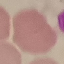

Malaria status: uninfected. Cell patch, automatically extracted from a larger field of view and resized to 64 × 64 pixels. Acquired by smartphone through the microscope eyepiece. Giemsa stain. Thin blood film.